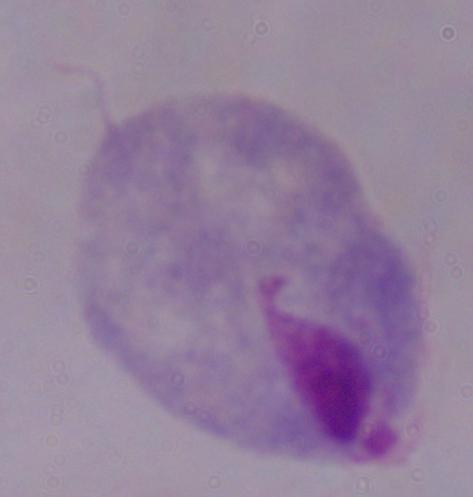

{
  "magnification": "1000x",
  "identification": "trichomonad",
  "modality": "micrograph"
}